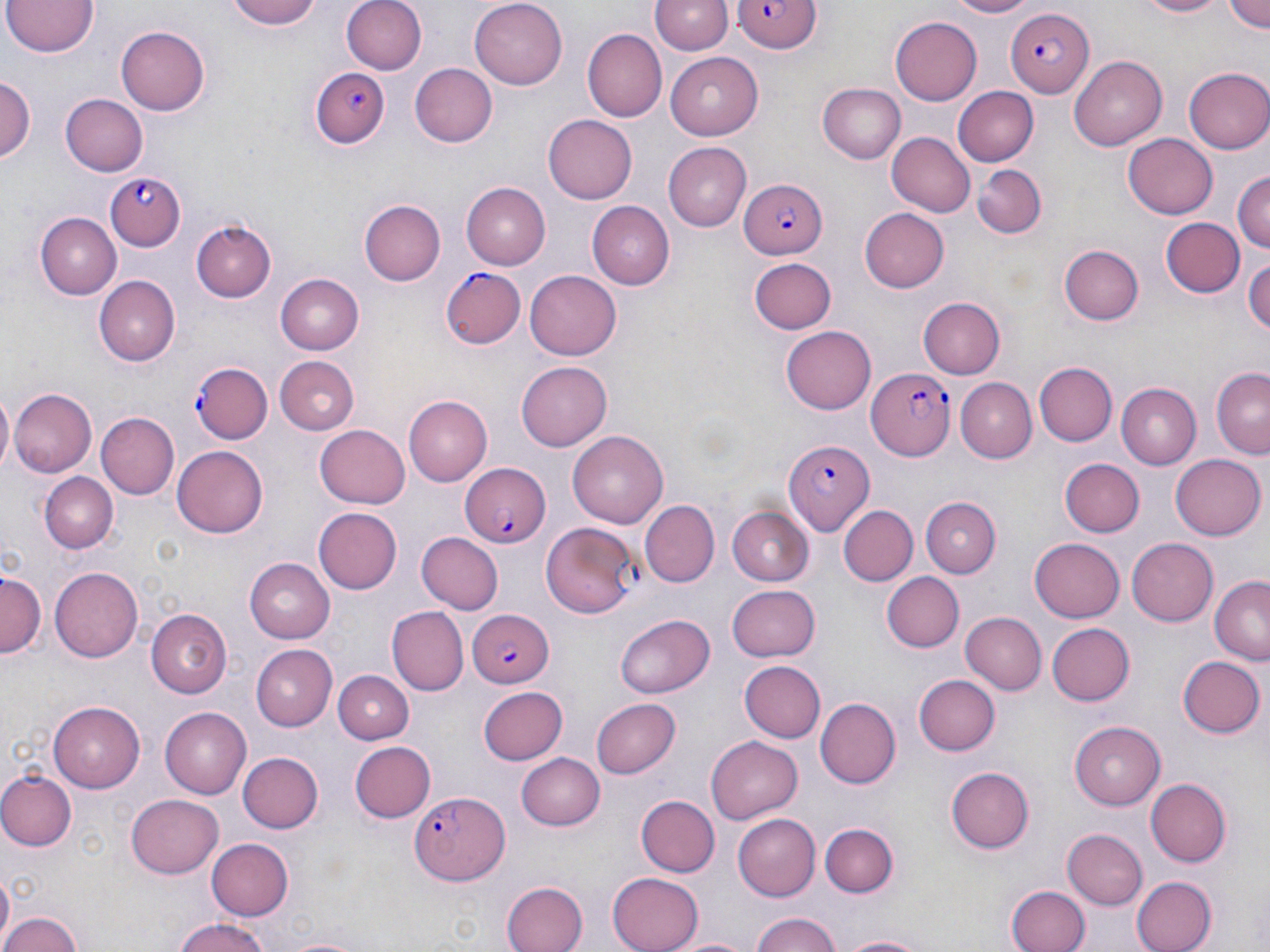 Approximate bounding boxes as named x1/y1/x2/y2 corners in pixels. Uninfected red blood cell locations: (x1=231, y1=0, x2=325, y2=30), (x1=343, y1=0, x2=428, y2=74), (x1=470, y1=0, x2=566, y2=89), (x1=943, y1=0, x2=1039, y2=17), (x1=1131, y1=0, x2=1232, y2=19), (x1=1223, y1=0, x2=1269, y2=34), (x1=3, y1=1, x2=98, y2=58), (x1=651, y1=1, x2=732, y2=56), (x1=890, y1=17, x2=983, y2=104), (x1=116, y1=25, x2=211, y2=115), (x1=582, y1=28, x2=666, y2=122), (x1=666, y1=52, x2=765, y2=140), (x1=1070, y1=57, x2=1167, y2=150), (x1=408, y1=62, x2=497, y2=147), (x1=1183, y1=66, x2=1270, y2=155), (x1=0, y1=74, x2=34, y2=170), (x1=817, y1=82, x2=906, y2=163), (x1=951, y1=85, x2=1036, y2=166), (x1=59, y1=92, x2=147, y2=175), (x1=543, y1=115, x2=638, y2=204), (x1=885, y1=131, x2=974, y2=217), (x1=1123, y1=134, x2=1218, y2=219), (x1=661, y1=142, x2=751, y2=230), (x1=972, y1=161, x2=1048, y2=238), (x1=1233, y1=170, x2=1268, y2=257), (x1=460, y1=181, x2=550, y2=270), (x1=360, y1=199, x2=445, y2=286), (x1=586, y1=201, x2=674, y2=290), (x1=859, y1=208, x2=949, y2=293), (x1=36, y1=213, x2=122, y2=298), (x1=1161, y1=218, x2=1245, y2=298), (x1=191, y1=220, x2=276, y2=302), (x1=1059, y1=245, x2=1144, y2=326), (x1=1244, y1=255, x2=1270, y2=341), (x1=748, y1=257, x2=836, y2=333), (x1=525, y1=269, x2=622, y2=360), (x1=274, y1=273, x2=364, y2=355), (x1=94, y1=277, x2=179, y2=366), (x1=917, y1=296, x2=1005, y2=379), (x1=780, y1=327, x2=876, y2=415), (x1=274, y1=354, x2=359, y2=434), (x1=517, y1=360, x2=612, y2=450), (x1=1035, y1=361, x2=1117, y2=447), (x1=1210, y1=368, x2=1269, y2=458), (x1=954, y1=377, x2=1036, y2=464), (x1=1116, y1=384, x2=1200, y2=468), (x1=9, y1=389, x2=96, y2=478), (x1=1, y1=393, x2=14, y2=472), (x1=404, y1=396, x2=491, y2=485), (x1=95, y1=412, x2=178, y2=500), (x1=316, y1=422, x2=410, y2=508), (x1=569, y1=432, x2=669, y2=528), (x1=173, y1=447, x2=268, y2=536), (x1=1170, y1=452, x2=1265, y2=539), (x1=1060, y1=457, x2=1144, y2=537), (x1=41, y1=474, x2=116, y2=552), (x1=921, y1=495, x2=1001, y2=575), (x1=640, y1=502, x2=718, y2=587), (x1=726, y1=506, x2=815, y2=585), (x1=840, y1=506, x2=917, y2=586), (x1=311, y1=507, x2=402, y2=595), (x1=417, y1=533, x2=502, y2=614), (x1=1124, y1=536, x2=1218, y2=627), (x1=1029, y1=538, x2=1126, y2=622), (x1=245, y1=559, x2=334, y2=641), (x1=51, y1=565, x2=147, y2=662), (x1=1, y1=571, x2=43, y2=660), (x1=884, y1=573, x2=964, y2=652), (x1=1208, y1=576, x2=1269, y2=664), (x1=727, y1=585, x2=822, y2=663), (x1=387, y1=607, x2=465, y2=694), (x1=146, y1=609, x2=232, y2=698), (x1=961, y1=612, x2=1046, y2=695), (x1=614, y1=613, x2=715, y2=698), (x1=1045, y1=621, x2=1132, y2=706), (x1=250, y1=645, x2=336, y2=729), (x1=1177, y1=655, x2=1264, y2=739), (x1=740, y1=662, x2=825, y2=742), (x1=333, y1=671, x2=414, y2=743), (x1=914, y1=674, x2=1000, y2=755), (x1=477, y1=686, x2=569, y2=766), (x1=590, y1=697, x2=680, y2=779), (x1=817, y1=697, x2=901, y2=788), (x1=48, y1=701, x2=145, y2=793), (x1=162, y1=707, x2=252, y2=798), (x1=1070, y1=719, x2=1167, y2=808), (x1=707, y1=734, x2=803, y2=820), (x1=350, y1=741, x2=435, y2=823), (x1=237, y1=751, x2=322, y2=834), (x1=517, y1=751, x2=605, y2=832), (x1=946, y1=766, x2=1033, y2=853), (x1=0, y1=771, x2=75, y2=850), (x1=1144, y1=780, x2=1229, y2=867), (x1=126, y1=794, x2=225, y2=877), (x1=634, y1=795, x2=719, y2=877), (x1=733, y1=813, x2=821, y2=900), (x1=820, y1=822, x2=899, y2=897), (x1=1061, y1=828, x2=1147, y2=911), (x1=207, y1=838, x2=293, y2=920), (x1=609, y1=871, x2=705, y2=952), (x1=0, y1=874, x2=13, y2=941), (x1=1131, y1=874, x2=1216, y2=952), (x1=502, y1=882, x2=587, y2=952), (x1=1005, y1=883, x2=1092, y2=952), (x1=747, y1=910, x2=845, y2=952), (x1=0, y1=911, x2=85, y2=952), (x1=170, y1=917, x2=276, y2=952), (x1=834, y1=933, x2=937, y2=952), (x1=671, y1=934, x2=756, y2=952), (x1=281, y1=935, x2=361, y2=952). Plasmodium falciparum-infected red blood cell locations: (x1=733, y1=0, x2=821, y2=51), (x1=1006, y1=8, x2=1095, y2=99), (x1=311, y1=68, x2=389, y2=151), (x1=107, y1=169, x2=185, y2=250), (x1=740, y1=177, x2=827, y2=258), (x1=438, y1=265, x2=528, y2=347), (x1=192, y1=362, x2=272, y2=443), (x1=868, y1=367, x2=956, y2=459), (x1=783, y1=440, x2=873, y2=532), (x1=459, y1=461, x2=549, y2=549), (x1=539, y1=523, x2=641, y2=618), (x1=467, y1=607, x2=552, y2=687), (x1=408, y1=791, x2=508, y2=884). Slide-level diagnosis: Plasmodium falciparum. May-Grünwald-Giemsa-stained preparation. Single field of view. Light microscopy. Captured at 1000x magnification. Thin blood film. Image is 1270×952 pixels.